Identify the blood parasite species.
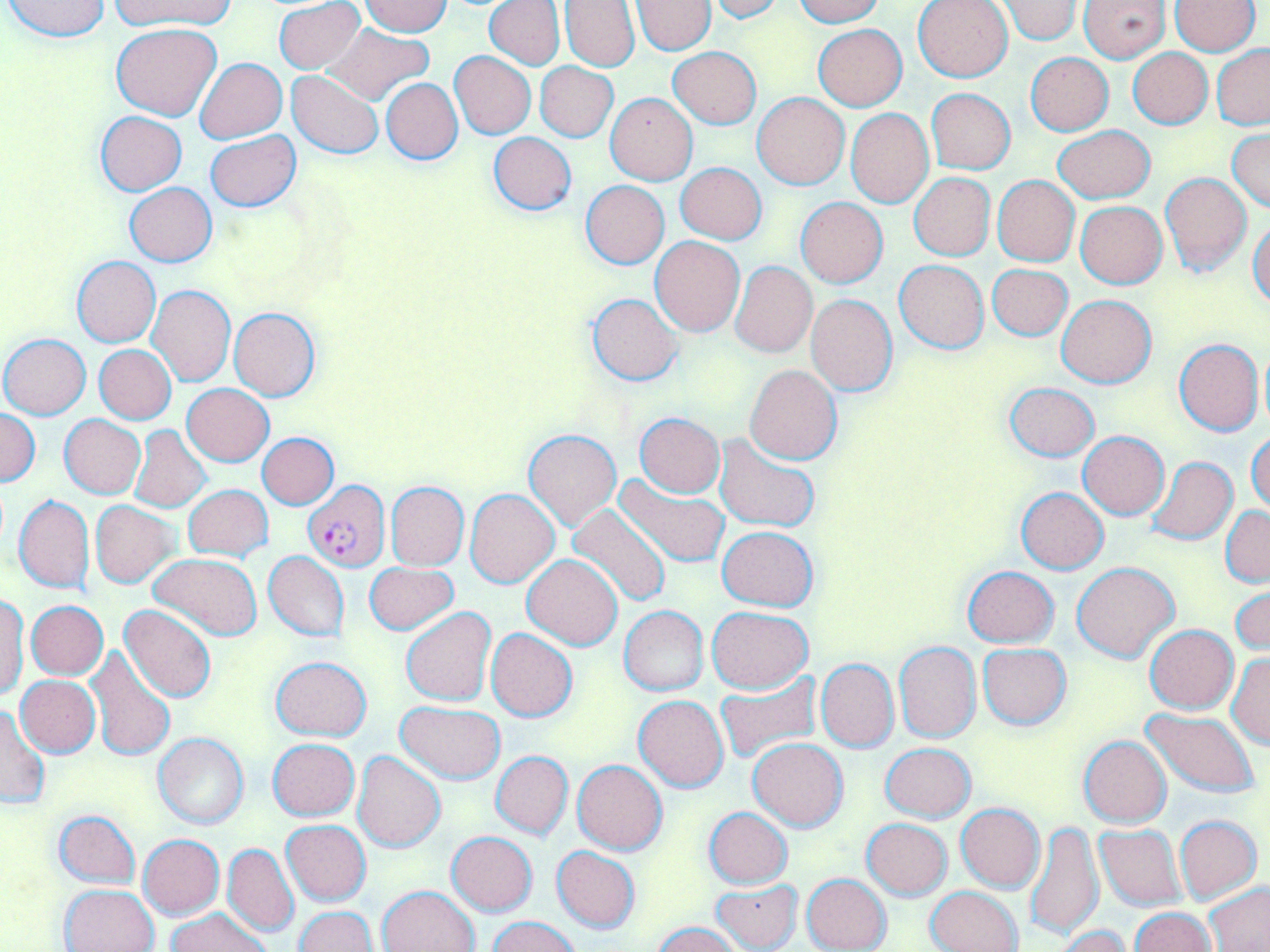
Plasmodium falciparum.

image size = 1270×952 pixels
stain = May-Grünwald-Giemsa
field of view = single
preparation = thin blood film
magnification = 1000x
uninfected red blood cell locations = approximate bounding boxes as [x1, y1, x2, y2] in pixels: [3, 0, 111, 42], [111, 0, 236, 30], [274, 0, 366, 74], [484, 0, 565, 69], [792, 0, 883, 26], [914, 0, 1014, 83], [1080, 0, 1170, 62], [1172, 0, 1261, 55], [361, 1, 454, 36], [560, 1, 640, 71], [632, 1, 715, 54], [709, 1, 789, 23], [998, 1, 1082, 45], [112, 23, 222, 121], [322, 23, 434, 105], [813, 24, 907, 111], [1212, 44, 1270, 129], [668, 47, 762, 129], [1127, 48, 1212, 129], [450, 51, 536, 138], [1025, 53, 1113, 136], [195, 57, 287, 143], [535, 62, 617, 141], [287, 71, 384, 159], [382, 78, 462, 164], [927, 88, 1015, 173], [606, 92, 697, 184], [751, 92, 849, 189], [846, 109, 934, 207], [95, 111, 186, 194], [1053, 124, 1156, 203], [1228, 128, 1269, 214], [205, 130, 300, 212], [488, 132, 576, 216], [676, 163, 766, 244], [1160, 172, 1254, 275], [908, 173, 995, 262], [993, 177, 1079, 266], [581, 180, 669, 269], [125, 182, 216, 266], [796, 197, 888, 288], [1076, 201, 1167, 288], [1249, 221, 1270, 310], [650, 236, 745, 336], [71, 255, 160, 347], [895, 259, 988, 353], [730, 261, 817, 357], [987, 263, 1073, 340], [149, 285, 236, 386], [587, 293, 683, 386], [1057, 294, 1156, 389], [805, 295, 898, 395], [229, 307, 321, 401], [0, 334, 90, 419], [1174, 338, 1264, 436], [1258, 343, 1270, 434], [94, 344, 176, 424], [744, 364, 842, 464], [1003, 382, 1099, 462], [182, 383, 273, 466], [0, 410, 40, 486], [634, 414, 725, 497], [59, 415, 146, 498], [129, 426, 211, 512], [524, 428, 621, 531], [1248, 430, 1270, 513], [1078, 432, 1169, 518], [257, 433, 338, 509], [715, 435, 821, 532], [1147, 456, 1238, 545], [613, 475, 731, 569], [386, 482, 469, 569], [184, 484, 273, 561], [1015, 487, 1110, 573], [465, 489, 559, 588], [14, 494, 95, 594], [90, 501, 177, 588], [567, 502, 672, 609], [1220, 506, 1269, 586], [716, 525, 819, 610], [264, 551, 349, 642], [150, 554, 263, 641], [522, 555, 622, 650], [363, 562, 459, 635], [1072, 562, 1179, 663], [962, 565, 1060, 648], [1230, 582, 1269, 658], [0, 594, 28, 699], [26, 600, 108, 679], [119, 604, 217, 705], [620, 606, 707, 696], [402, 607, 495, 705], [708, 607, 811, 693], [1145, 625, 1238, 713], [486, 628, 577, 721], [895, 642, 982, 743], [978, 642, 1072, 729], [87, 646, 176, 762], [1226, 653, 1269, 749], [271, 655, 372, 741], [816, 658, 899, 752], [714, 672, 820, 764], [16, 676, 101, 756], [633, 694, 728, 792], [396, 702, 507, 782], [0, 704, 49, 809], [1141, 709, 1258, 798], [153, 733, 248, 829], [1078, 735, 1171, 828], [268, 738, 358, 820], [748, 738, 848, 831], [881, 743, 975, 822], [352, 751, 447, 852], [490, 751, 573, 839], [573, 759, 667, 855], [956, 803, 1046, 892], [704, 807, 792, 888], [53, 810, 141, 888], [1175, 815, 1262, 903], [862, 818, 952, 899], [1025, 819, 1105, 939], [281, 820, 371, 906], [1094, 824, 1185, 911], [447, 831, 538, 915], [137, 834, 224, 919], [223, 844, 299, 938], [551, 846, 640, 932], [802, 873, 891, 952], [712, 878, 803, 950], [1204, 882, 1270, 951], [60, 883, 159, 952], [379, 884, 479, 952], [927, 886, 1021, 952], [295, 906, 377, 951], [1129, 907, 1215, 951], [168, 908, 268, 952], [487, 915, 582, 952], [653, 922, 741, 952], [1056, 926, 1132, 952]
Plasmodium falciparum-infected red blood cell locations = approximate bounding boxes as [x1, y1, x2, y2] in pixels: [302, 482, 389, 570]
modality = light microscopy